Outline each blood parasite and name the species.
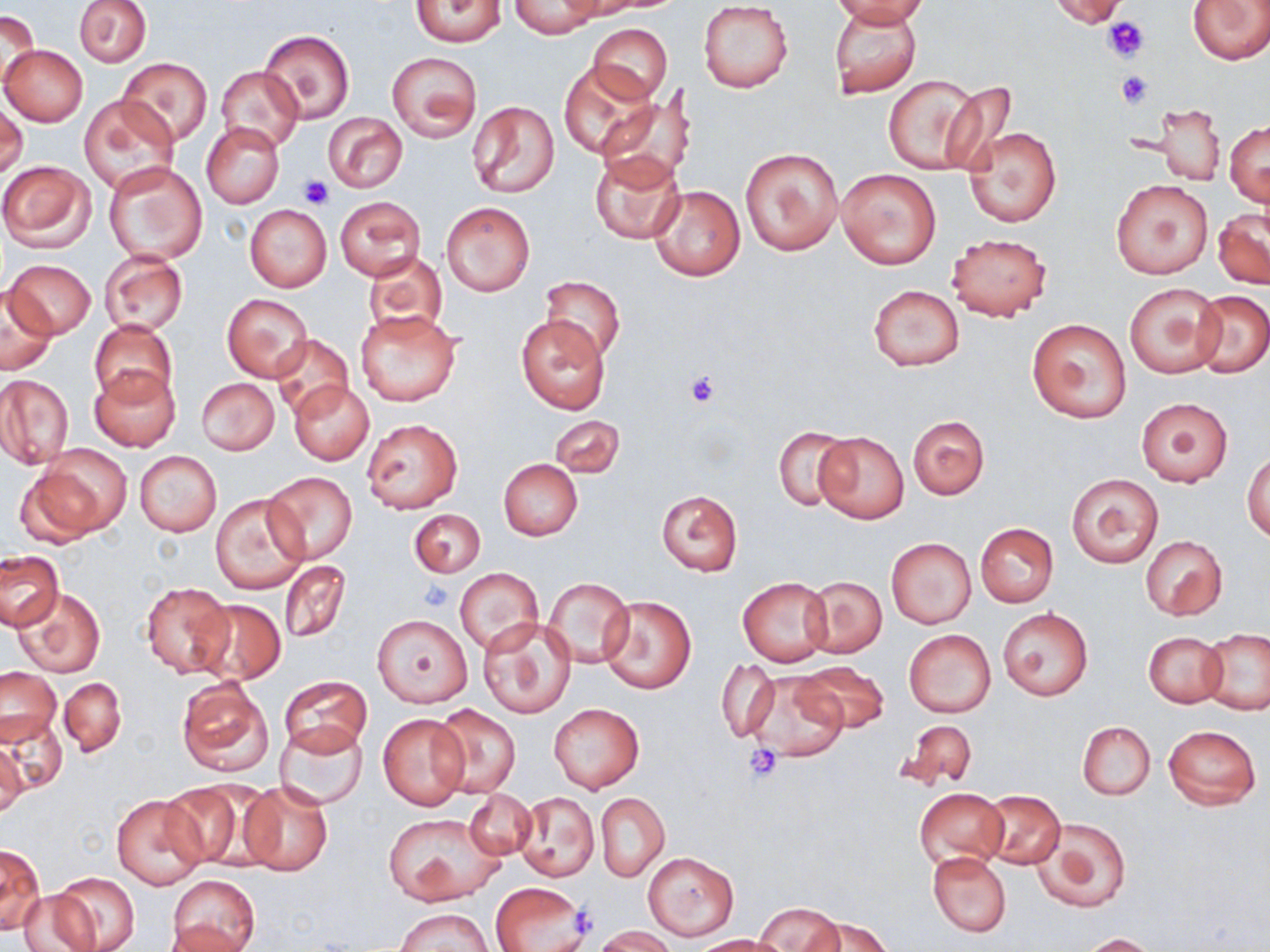
No blood parasites observed.

{
  "slide_level_diagnosis": "negative for blood parasites",
  "field_of_view": "one of a larger specimen",
  "stain": "May-Grünwald-Giemsa",
  "image_size": "1270×952 pixels",
  "modality": "light microscopy",
  "preparation": "thin blood film",
  "platelet_locations": "approximate bounding boxes as (x1, y1, x2, y2) in pixels: (1102, 16, 1150, 64), (1115, 71, 1151, 109), (297, 174, 332, 207), (682, 368, 723, 408), (419, 580, 453, 611), (746, 745, 785, 782), (570, 903, 602, 941)",
  "magnification": "1000x",
  "uninfected_red_blood_cell_locations": "approximate bounding boxes as (x1, y1, x2, y2) in pixels: (74, 0, 151, 66), (410, 0, 508, 47), (830, 0, 934, 26), (1048, 0, 1130, 29), (1186, 0, 1270, 65), (698, 1, 793, 93), (509, 3, 602, 36), (0, 10, 38, 90), (829, 10, 923, 98), (588, 23, 673, 104), (260, 29, 354, 122), (0, 45, 87, 126), (386, 52, 481, 142), (117, 58, 213, 147), (559, 62, 659, 158), (216, 66, 303, 152), (884, 75, 983, 175), (936, 81, 1018, 175), (595, 94, 693, 189), (78, 95, 179, 194), (0, 100, 27, 178), (468, 100, 559, 199), (1143, 103, 1227, 185), (323, 112, 408, 193), (1226, 120, 1269, 207), (200, 122, 284, 208), (965, 127, 1061, 228), (738, 145, 844, 256), (589, 151, 686, 246), (0, 160, 95, 252), (103, 160, 207, 265), (837, 169, 941, 269), (1112, 179, 1212, 280), (649, 184, 746, 281), (336, 197, 424, 280), (441, 202, 534, 296), (245, 205, 331, 293), (1212, 208, 1270, 290), (946, 232, 1052, 321), (361, 250, 449, 336), (99, 252, 188, 336), (6, 259, 95, 338), (538, 275, 626, 363), (1125, 282, 1224, 378), (867, 284, 965, 371), (1, 286, 57, 374), (1191, 291, 1269, 377), (222, 293, 314, 382), (355, 310, 461, 406), (516, 315, 612, 414), (1026, 318, 1133, 423), (89, 320, 177, 409), (271, 334, 354, 418), (90, 366, 179, 452), (0, 375, 74, 468), (196, 378, 279, 454), (288, 380, 374, 465), (1136, 398, 1233, 486), (549, 414, 624, 477), (909, 415, 989, 499), (362, 419, 462, 514), (772, 427, 853, 512), (814, 429, 909, 524), (35, 443, 131, 532), (134, 450, 221, 536), (1244, 450, 1270, 543), (498, 459, 583, 540), (14, 466, 106, 549), (261, 470, 359, 565), (1066, 473, 1164, 567), (655, 491, 743, 577), (210, 492, 309, 594), (410, 509, 485, 577), (975, 523, 1059, 608), (1141, 534, 1227, 620), (885, 537, 976, 629), (1, 551, 61, 629), (279, 561, 350, 640), (454, 567, 543, 655), (804, 575, 887, 658), (543, 577, 633, 669), (738, 577, 831, 666), (140, 581, 235, 679), (13, 587, 105, 678), (598, 594, 695, 695), (191, 598, 284, 685), (999, 608, 1092, 701), (373, 614, 472, 707), (478, 617, 576, 718), (904, 628, 996, 718), (1199, 628, 1270, 715), (1143, 631, 1228, 707), (717, 660, 779, 741), (796, 662, 889, 732), (1, 666, 61, 747), (745, 671, 849, 763), (278, 674, 373, 755), (60, 677, 126, 758), (176, 677, 273, 779), (548, 702, 646, 794), (429, 703, 521, 798), (378, 712, 470, 809), (2, 716, 68, 795), (897, 720, 977, 793), (276, 721, 367, 809), (1078, 721, 1155, 800), (1163, 724, 1262, 809), (0, 738, 27, 820), (155, 781, 257, 869), (238, 781, 333, 876), (916, 787, 1008, 871), (463, 789, 536, 861), (982, 790, 1065, 868), (514, 791, 599, 883), (596, 793, 669, 881), (112, 795, 207, 888), (383, 812, 506, 906), (1033, 816, 1131, 912), (0, 844, 43, 935), (927, 851, 1011, 937), (642, 853, 739, 939), (48, 871, 140, 952), (167, 875, 260, 948), (490, 881, 588, 952), (17, 890, 95, 952), (754, 903, 846, 951), (395, 907, 492, 952), (809, 916, 893, 952), (164, 920, 254, 951), (595, 926, 678, 952), (1079, 933, 1157, 952), (692, 934, 788, 951)"
}